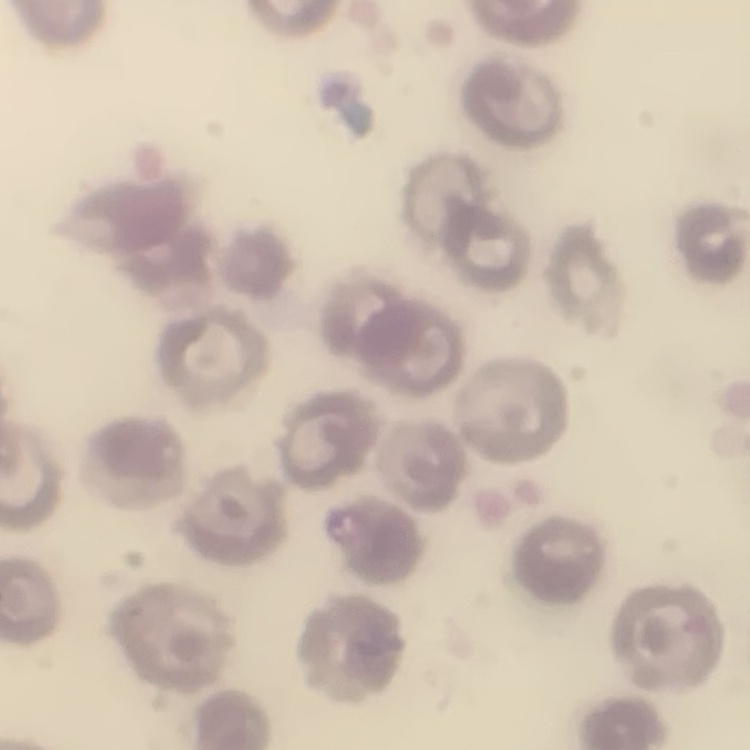

erythrocyte_morphology: no rouleaux formation
stain: Field's or Giemsa
preparation: thin peripheral smear
image_type: one tile cut from a larger photomicrograph